Assess this cell for malaria.
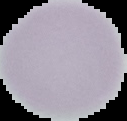

Uninfected.

image size = 127×121 pixels
preparation = thin blood smear
image type = segmented cell region with the area outside set to black